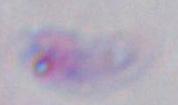

Summary:
  - Identification: Toxoplasma gondii
  - Modality: micrograph
  - Magnification: 1000x